Comment on the morphology of the erythrocytes.
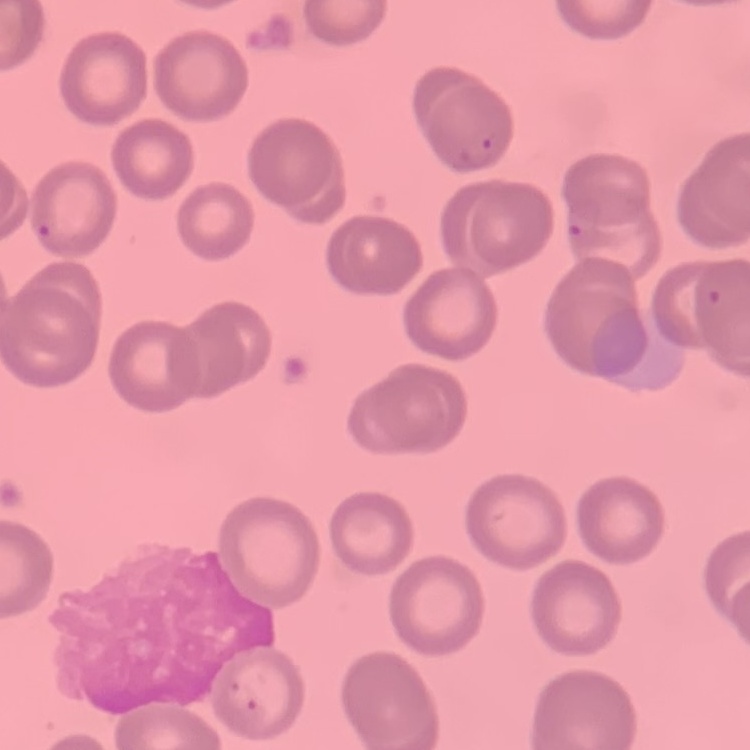
They show no rouleaux formation.

Summary:
  - Preparation: thin peripheral smear
  - Stain: Field's or Giemsa
  - Image type: square crop of a larger photomicrograph